Assess this cell for malaria.
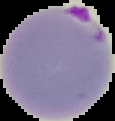
Parasitized.

Summary:
  - Image size: 115×121 pixels
  - Image type: segmented cell region on a black background
  - Preparation: thin blood film